Name the blood parasite species.
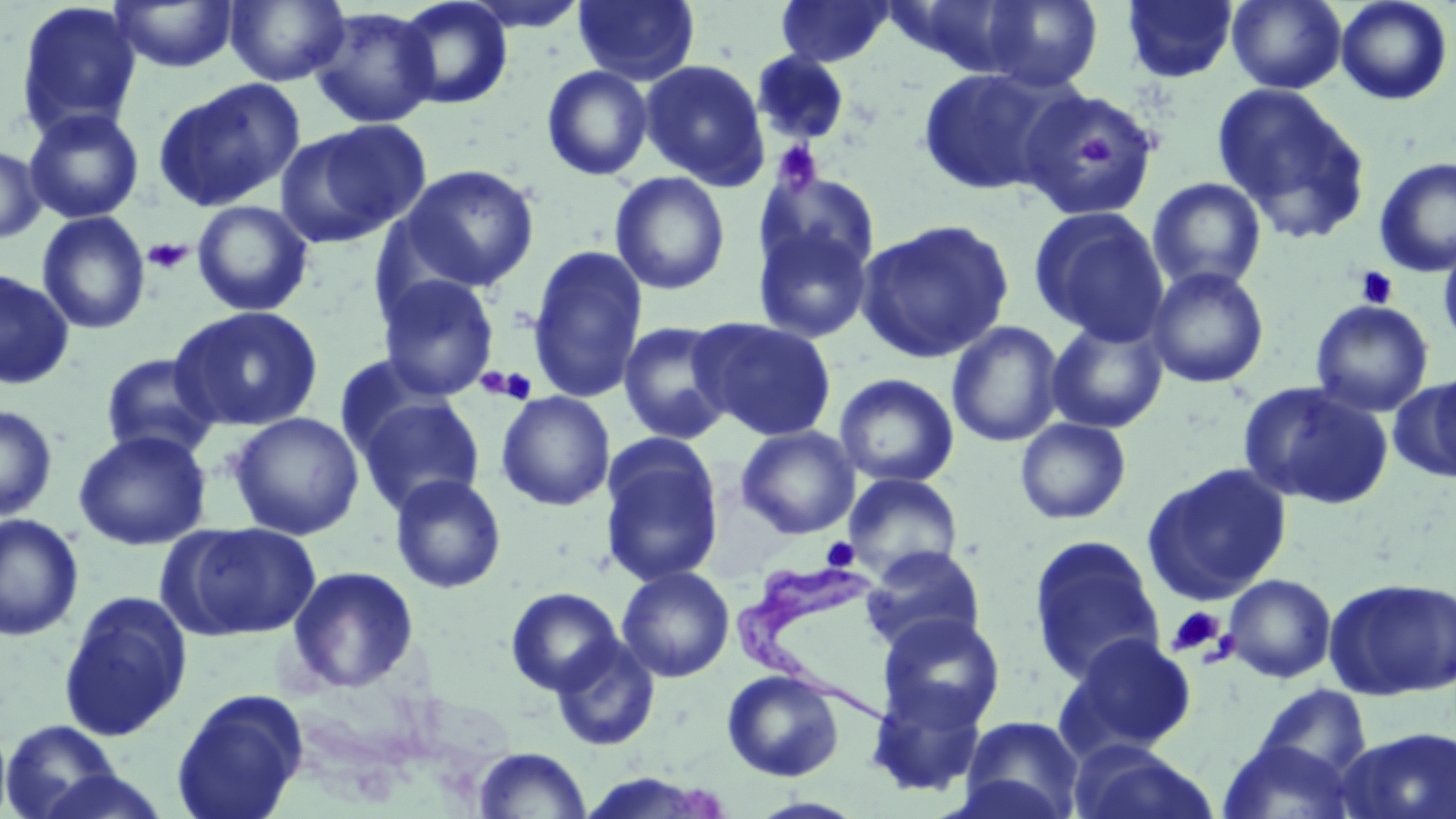

Trypanosoma brucei.

Approximate bounding boxes as (x1, y1, x2, y2) in pixels. Platelet locations: (1078, 136, 1122, 167), (774, 140, 823, 191), (143, 238, 191, 274), (1354, 266, 1399, 310), (482, 367, 538, 405), (821, 537, 859, 570), (1165, 606, 1228, 658). Uninfected red blood cell locations: (224, 0, 350, 86), (392, 0, 514, 110), (459, 0, 592, 33), (573, 0, 700, 85), (775, 0, 895, 67), (885, 0, 1037, 78), (981, 0, 1103, 92), (1120, 0, 1239, 84), (1226, 0, 1347, 93), (15, 1, 142, 139), (109, 1, 239, 73), (1335, 1, 1454, 105), (309, 7, 441, 129), (751, 52, 851, 147), (639, 58, 771, 190), (541, 65, 654, 181), (916, 66, 1068, 196), (152, 79, 305, 212), (1212, 83, 1371, 243), (1017, 87, 1161, 222), (24, 108, 145, 224), (275, 122, 427, 248), (0, 145, 46, 245), (1373, 156, 1456, 278), (400, 164, 540, 292), (758, 170, 882, 279), (609, 171, 731, 295), (1146, 177, 1267, 293), (191, 200, 314, 316), (1028, 206, 1170, 345), (37, 211, 151, 335), (855, 219, 1015, 364), (752, 224, 874, 343), (1438, 231, 1456, 356), (527, 245, 648, 403), (1146, 266, 1270, 389), (0, 268, 74, 389), (377, 274, 499, 401), (1310, 299, 1434, 417), (170, 305, 324, 431), (693, 318, 837, 441), (1046, 318, 1169, 434), (618, 320, 736, 445), (946, 321, 1065, 448), (100, 352, 221, 461), (834, 373, 959, 488), (1391, 373, 1456, 483), (1239, 381, 1393, 510), (496, 391, 615, 511), (356, 395, 486, 516), (0, 405, 58, 521), (228, 412, 364, 540), (1014, 417, 1132, 525), (736, 425, 860, 539), (72, 429, 212, 551), (600, 438, 724, 587), (1142, 463, 1293, 604), (844, 472, 963, 580), (389, 474, 507, 594), (0, 513, 84, 641), (167, 522, 321, 642), (1028, 535, 1166, 686), (862, 545, 986, 653), (616, 565, 735, 682), (285, 566, 420, 693), (1224, 573, 1337, 683), (1324, 577, 1456, 700), (506, 587, 623, 696), (58, 591, 193, 742), (878, 613, 1005, 733), (1060, 633, 1198, 757), (551, 635, 660, 752), (721, 670, 845, 781), (865, 680, 990, 799), (1252, 684, 1372, 782), (171, 689, 309, 819), (958, 715, 1085, 819), (1, 719, 125, 818), (0, 720, 12, 819), (1336, 726, 1456, 819), (1216, 738, 1360, 819), (1068, 740, 1219, 819), (473, 747, 591, 819), (28, 768, 174, 818), (577, 773, 726, 818). Trypanosoma brucei locations: (738, 557, 900, 715). Light microscopy. Single field of view. Thin blood smear. Image is 1456×819 pixels. 1000x magnification. May-Grünwald-Giemsa-stained preparation.